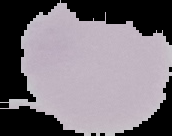
Segmented cell region on a black background. Image is 172×136 pixels. From a thin blood smear. Result: negative for malaria parasites.